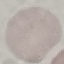
Summary:
  - Result: no malaria parasites detected
  - Preparation: thin blood film
  - Capture: smartphone camera at the microscope eyepiece
  - Image type: cell patch, automatically extracted from a larger field of view and resized to 64 × 64 pixels
  - Stain: Giemsa